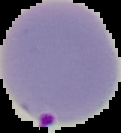

Summary:
  - Result: Plasmodium parasites identified
  - Preparation: thin blood smear
  - Image size: 121×133 pixels
  - Image type: segmented cell region on a black background